Report the malaria status of this cell.
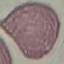
It is uninfected.

preparation = thin blood smear
image type = automatically extracted cell patch, resized to 64 × 64 pixels
stain = Giemsa
capture = smartphone through the microscope eyepiece